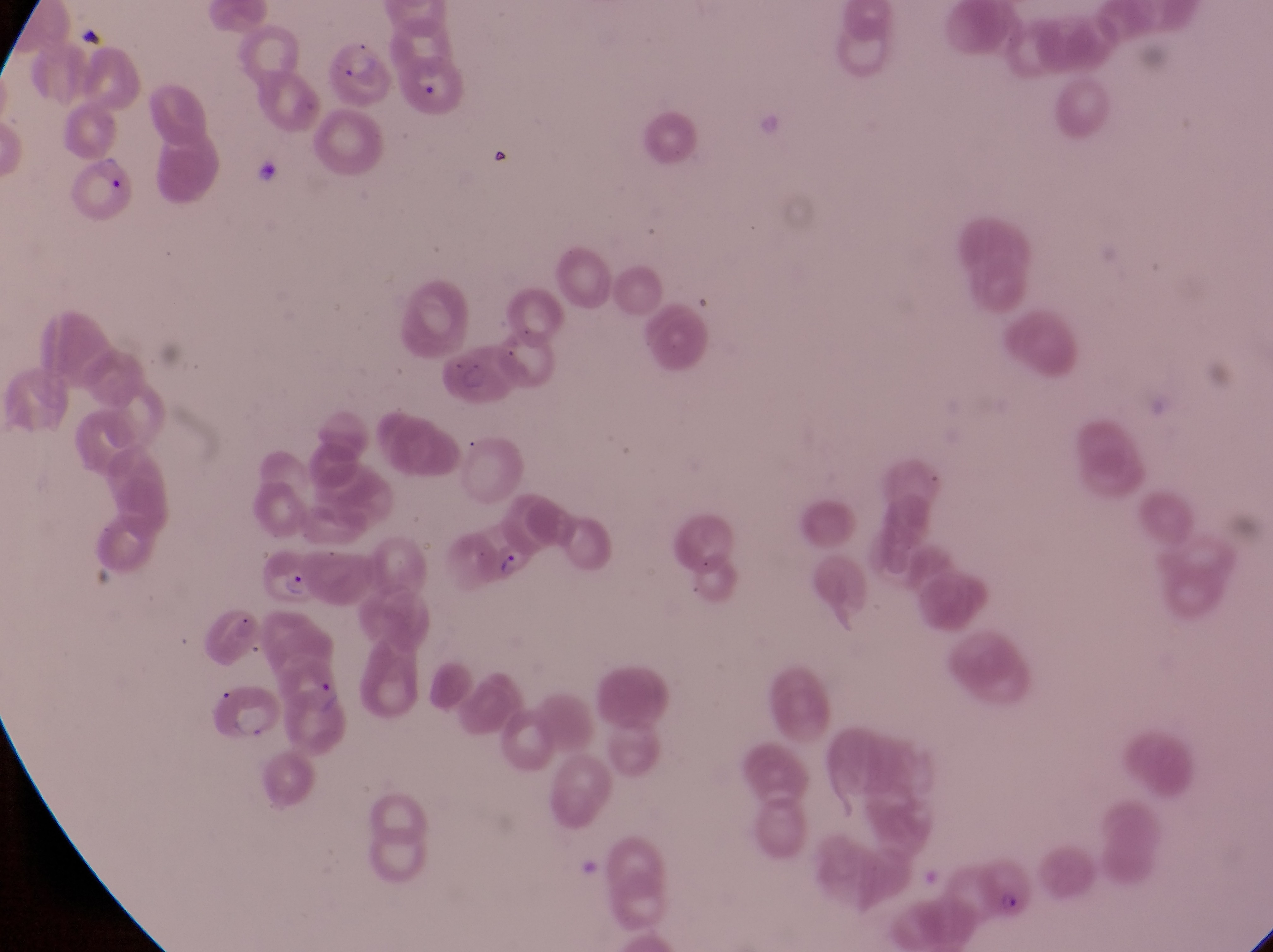

Approximate bounding boxes as left top right bottom in pixels. Parasitised red blood cell locations: 328 41 397 107; 58 157 138 219; 257 545 315 608; 978 856 1036 918. Artifact (platelet-like body, stain precipitate, or debris) locations: 495 547 534 587. Image is 1273×952 pixels. One field of view. Thin blood smear. Collected in Uganda. Captured by a smartphone held over the eyepiece of an Olympus CX-23 microscope. At a magnification of 1000x.